Report the malaria status of this cell.
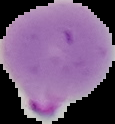
Parasitized.

Summary:
  - Preparation: thin blood smear
  - Image size: 115×124 pixels
  - Image type: cell region segmented out of the field of view; surrounding area masked to black